Report the malaria status of this cell.
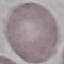
It is uninfected.

capture = smartphone camera at the microscope eyepiece
stain = Giemsa
image type = automatically extracted cell patch, resized to 64 × 64 pixels
preparation = thin blood smear